Name the parasite shown.
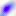

This is Toxoplasma gondii.

modality = micrograph
magnification = 400x